Assess this cell for malaria.
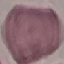

It is uninfected.

capture = smartphone through the microscope eyepiece
preparation = thin smear
stain = Giemsa
image type = automatically extracted cell patch, resized to 64 × 64 pixels